Point out leukocytes.
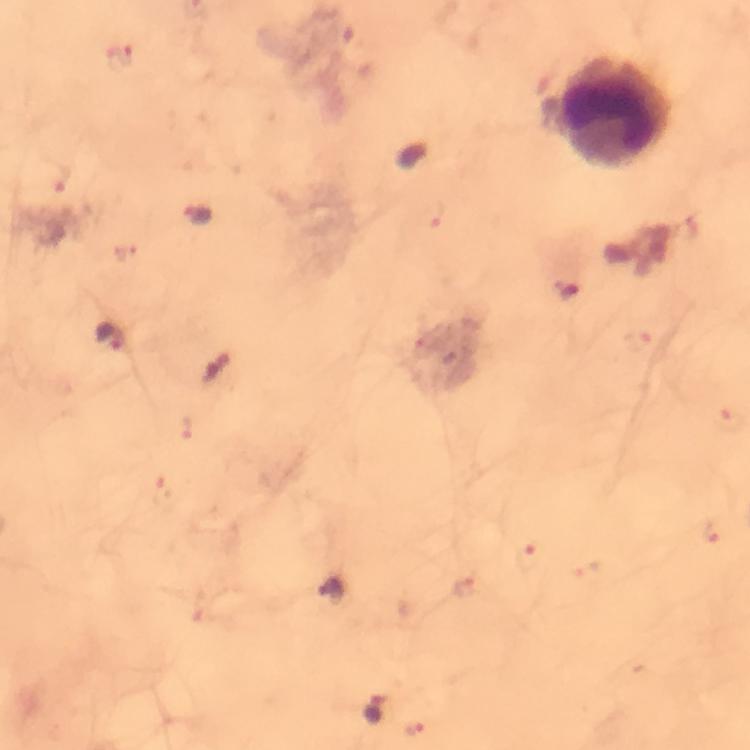

Approximate centers as (x, y) in pixels.
Leukocytes: (612, 113).

immersion oil = used
Plasmodium parasite locations = approximate centers as (x, y) in pixels: (198, 216), (569, 288), (112, 337), (215, 371), (330, 590), (375, 712)
stain = Giemsa
magnification = 100x
image size = 750×750 pixels
capture = smartphone photograph through a microscope
cropped from = one field of view
context = from a malaria diagnostic workup
preparation = thick blood smear